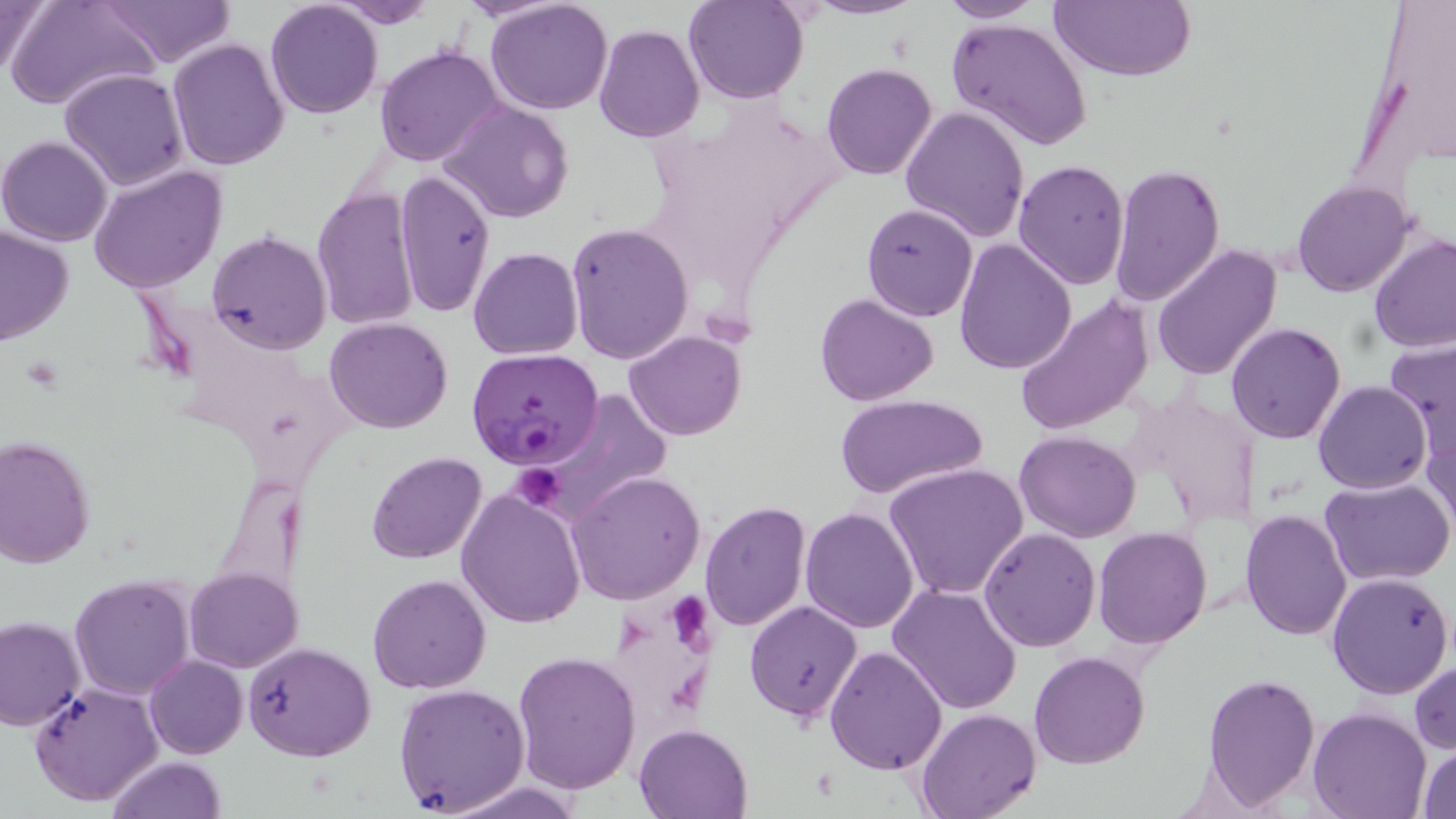

Approximate bounding boxes as [x1, y1, x2, y2] in pixels. Plasmodium falciparum-infected red blood cell locations: [468, 349, 604, 472]. Platelet locations: [509, 465, 566, 515], [668, 587, 712, 654]. Uninfected red blood cell locations: [0, 0, 52, 86], [8, 0, 157, 112], [98, 0, 236, 68], [263, 0, 383, 120], [328, 0, 441, 28], [684, 0, 809, 104], [803, 0, 924, 20], [937, 0, 1048, 24], [1048, 0, 1197, 82], [485, 1, 613, 115], [948, 17, 1093, 149], [592, 24, 705, 145], [166, 39, 290, 172], [375, 44, 504, 168], [821, 63, 939, 182], [59, 68, 190, 192], [830, 79, 1024, 216], [440, 101, 574, 223], [900, 105, 1030, 243], [0, 135, 113, 246], [1012, 161, 1130, 289], [1108, 161, 1226, 309], [87, 164, 228, 294], [392, 169, 495, 317], [1291, 180, 1416, 299], [310, 185, 421, 331], [860, 204, 980, 325], [565, 222, 694, 364], [0, 227, 75, 345], [207, 230, 330, 355], [1368, 233, 1456, 352], [952, 238, 1077, 376], [1151, 242, 1281, 382], [468, 247, 584, 360], [814, 293, 940, 407], [1011, 294, 1155, 438], [325, 316, 453, 434], [1226, 322, 1346, 444], [626, 329, 746, 441], [1383, 336, 1456, 460], [1313, 381, 1431, 495], [540, 389, 675, 521], [1124, 389, 1260, 530], [836, 393, 986, 497], [1423, 422, 1455, 535], [1014, 429, 1141, 542], [1, 437, 97, 569], [366, 450, 488, 564], [883, 462, 1028, 599], [213, 468, 308, 601], [566, 471, 705, 604], [1321, 476, 1455, 586], [455, 487, 587, 630], [700, 500, 811, 631], [799, 507, 921, 632], [1241, 509, 1353, 642], [1094, 527, 1211, 648], [978, 528, 1101, 652], [185, 566, 304, 673], [1326, 572, 1453, 699], [367, 573, 492, 694], [69, 574, 197, 701], [887, 584, 1023, 717], [744, 600, 863, 725], [0, 615, 86, 728], [242, 641, 377, 761], [825, 645, 946, 776], [512, 651, 641, 795], [1029, 651, 1149, 769], [144, 655, 247, 759], [1410, 662, 1455, 754], [1202, 673, 1320, 808], [29, 682, 164, 806], [393, 683, 530, 814], [1308, 708, 1431, 819], [915, 709, 1040, 819], [633, 722, 754, 819], [1417, 744, 1456, 818], [108, 756, 227, 819]. Slide-level diagnosis: Plasmodium falciparum. Thin blood film. Image is 1456×819 pixels. Light microscopy. May-Grünwald-Giemsa-stained preparation. One field of a larger specimen. Captured at 1000x magnification.